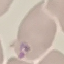 Malaria status: parasitized. Giemsa stain. Automatically extracted cell patch, resized to 64 × 64 pixels. Acquired by smartphone through the microscope eyepiece. Thin blood smear.